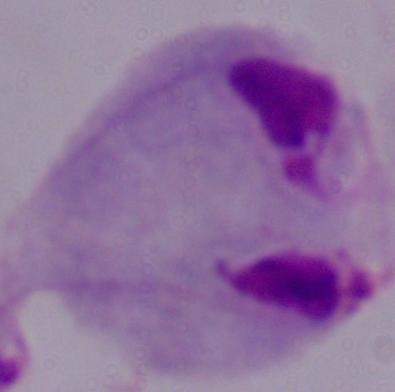
{
  "magnification": "1000x",
  "modality": "micrograph",
  "identification": "trichomonad"
}